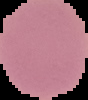

Summary:
  - Preparation: thin blood smear
  - Result: no Plasmodium parasites seen
  - Image type: cell region segmented out of the field of view; surrounding area masked to black
  - Image size: 88×100 pixels